Give the position of every Plasmodium parasite visible.
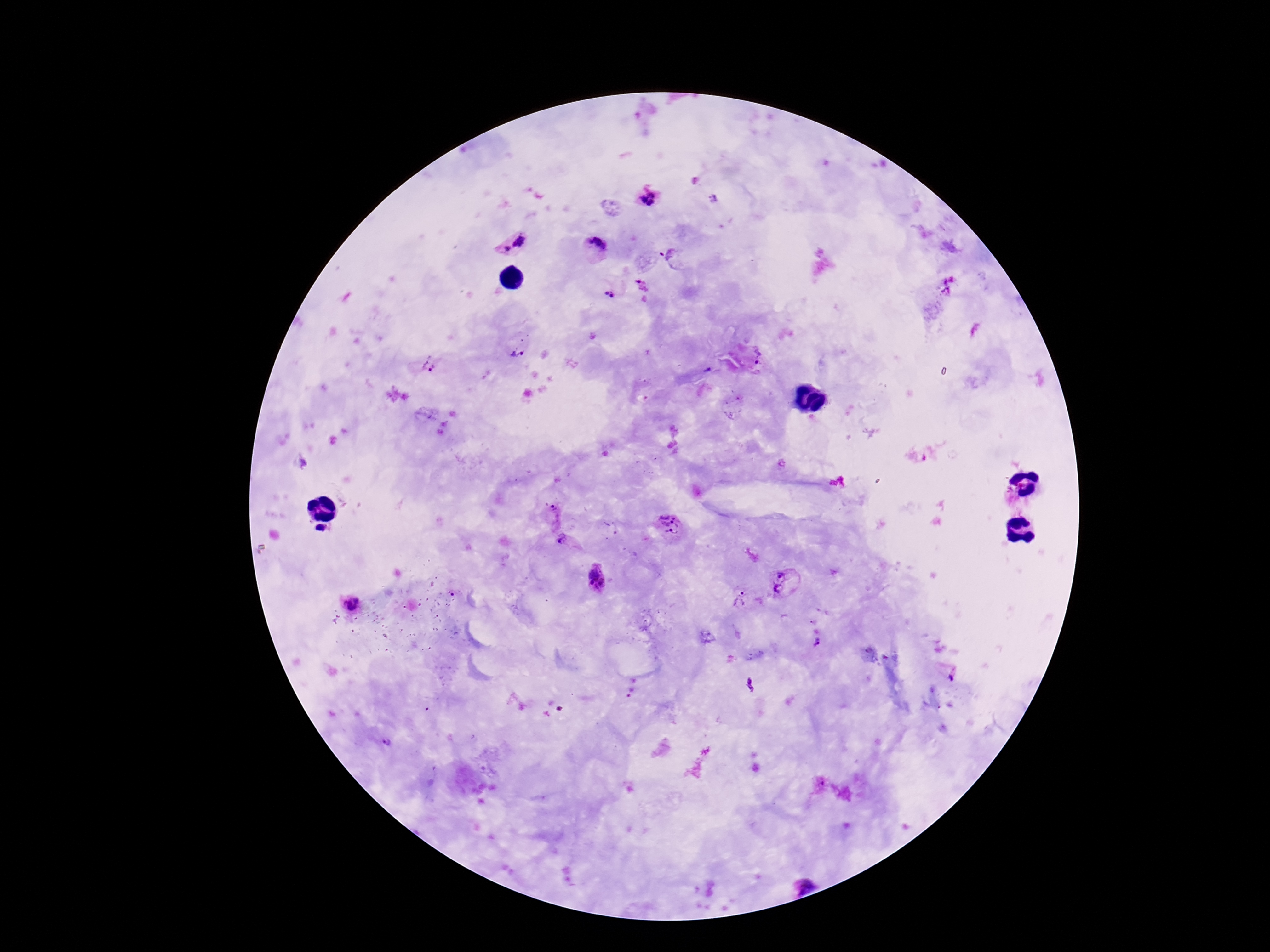

Approximate centers as {x, y} in pixels.
Plasmodium parasites: {651, 194}, {712, 199}, {643, 200}, {651, 204}, {520, 242}, {593, 249}, {507, 250}, {672, 255}, {641, 285}, {947, 286}, {605, 293}, {612, 296}, {518, 350}, {760, 359}, {430, 367}, {554, 513}, {671, 526}, {323, 532}, {561, 541}, {780, 576}, {597, 577}, {778, 588}, {452, 594}, {740, 600}, {350, 604}, {813, 622}, {817, 641}, {867, 651}, {951, 676}, {750, 685}, {630, 688}, {386, 744}, {806, 885}.

Summary:
  - Stain: Giemsa
  - Field of view: single
  - Capture: smartphone camera through the microscope eyepiece
  - Patient malaria status: positive
  - Preparation: thick peripheral-blood smear
  - Magnification: 100x
  - Image size: 1270×952 pixels